State which parasite is depicted.
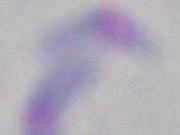
Toxoplasma gondii.

Summary:
  - Modality: micrograph
  - Magnification: 1000x